Identify the parasite.
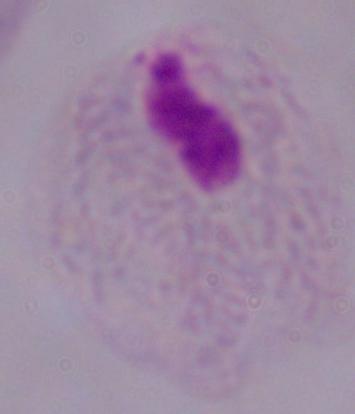

This is a trichomonad.

Summary:
  - Modality: micrograph
  - Magnification: 1000x